Classify this cell by malaria status.
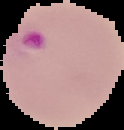
Parasitized.

{
  "image_type": "cell region segmented out of the field of view; surrounding area masked to black",
  "image_size": "124×130 pixels",
  "preparation": "thin blood smear"
}